Describe the morphology of the red blood cells.
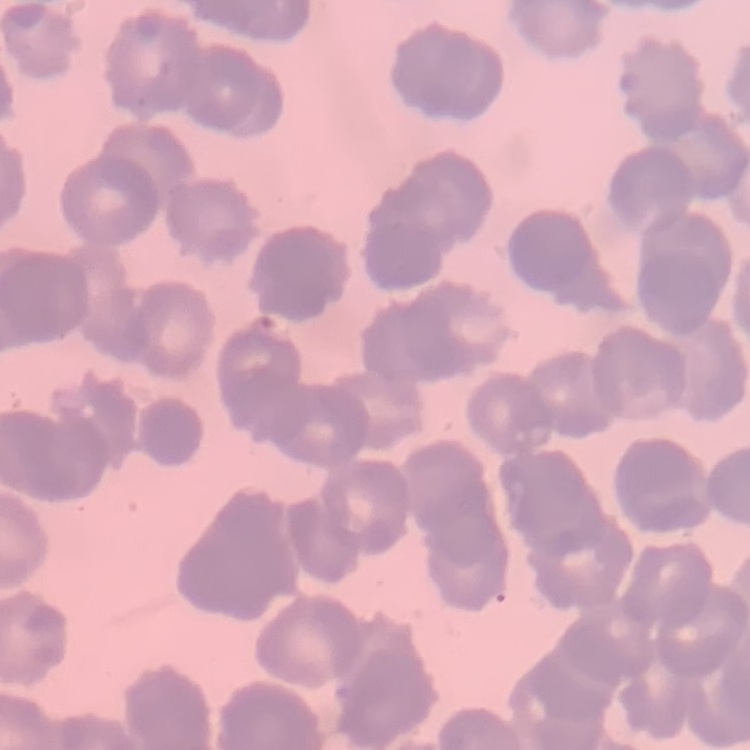
They show rouleaux formation.

Summary:
  - Image type: square crop of a larger photomicrograph
  - Stain: Field's or Giemsa
  - Preparation: thin peripheral smear